Identify the parasite.
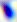

This is Toxoplasma gondii.

magnification = 400x
modality = photomicrograph